Identify the parasite.
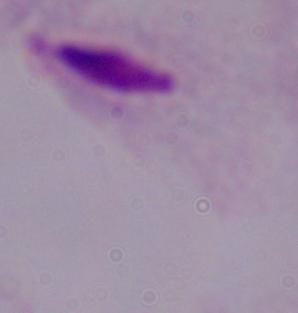
A trichomonad.

magnification = 1000x
modality = photomicrograph